Describe the morphology of the erythrocytes.
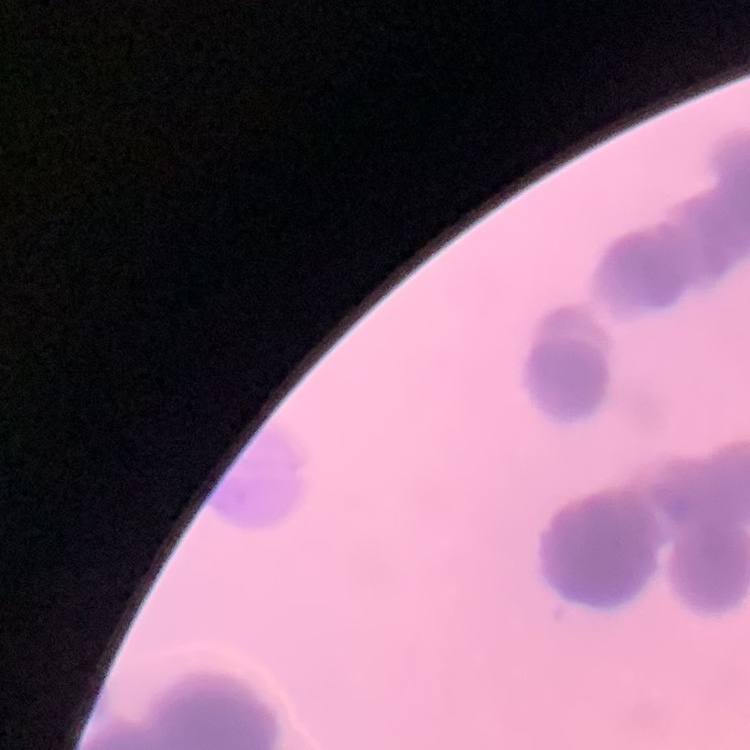
Rouleaux formation.

Thin blood film. Stained with either Field's or Giemsa. One tile cut from a larger photomicrograph.